Name the blood parasite species.
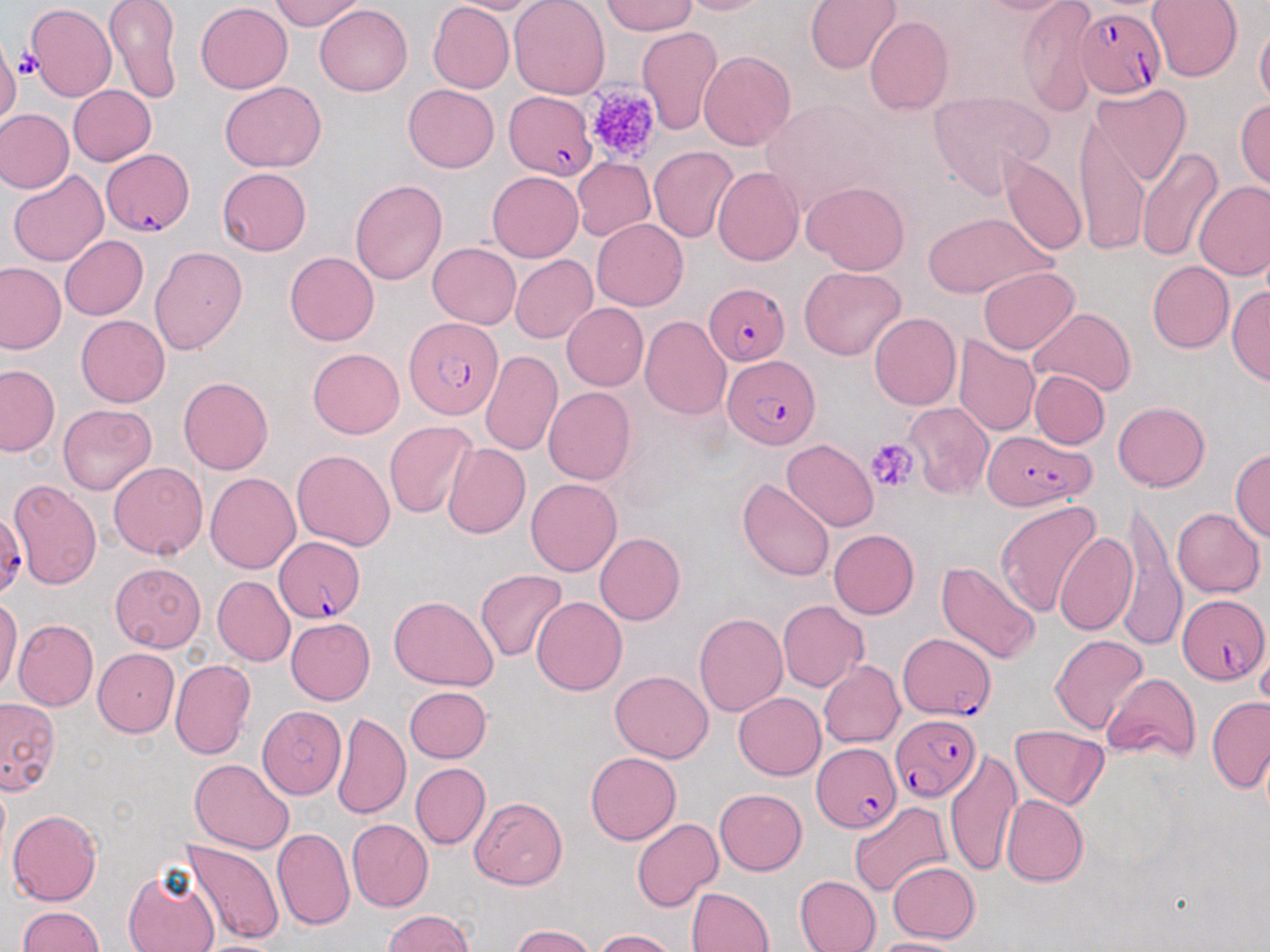

Plasmodium falciparum.

Approximate bounding boxes as [x1, y1, x2, y2] in pixels. Platelet locations: [15, 50, 39, 81], [582, 82, 664, 164], [866, 438, 919, 493]. Plasmodium falciparum-infected red blood cell locations: [1076, 7, 1165, 99], [503, 91, 597, 180], [102, 149, 194, 236], [703, 281, 789, 369], [404, 317, 505, 421], [722, 355, 819, 448], [983, 429, 1096, 510], [0, 512, 25, 597], [274, 536, 366, 622], [1178, 594, 1268, 685], [897, 633, 993, 719], [893, 711, 981, 802], [811, 741, 900, 833]. Uninfected red blood cell locations: [104, 0, 182, 104], [269, 0, 365, 31], [444, 0, 548, 14], [509, 0, 610, 100], [673, 0, 774, 15], [804, 0, 902, 74], [965, 0, 1079, 15], [1016, 0, 1098, 116], [1146, 0, 1242, 81], [196, 1, 293, 93], [428, 1, 514, 93], [602, 1, 698, 36], [26, 3, 116, 100], [315, 3, 412, 97], [865, 16, 953, 117], [1255, 20, 1270, 110], [636, 26, 724, 134], [0, 39, 20, 127], [698, 50, 797, 150], [219, 81, 327, 171], [404, 84, 499, 172], [1089, 84, 1191, 188], [69, 85, 156, 166], [928, 91, 1053, 196], [757, 98, 891, 214], [1234, 98, 1270, 190], [1, 109, 72, 193], [1074, 114, 1148, 255], [1136, 146, 1225, 262], [649, 147, 740, 244], [1000, 154, 1086, 258], [571, 156, 655, 242], [217, 167, 312, 255], [712, 167, 804, 266], [7, 171, 108, 266], [487, 171, 583, 262], [350, 179, 448, 285], [801, 181, 909, 274], [1193, 181, 1270, 281], [923, 211, 1053, 297], [591, 219, 687, 311], [60, 236, 148, 320], [427, 242, 521, 328], [149, 246, 247, 354], [284, 251, 379, 345], [510, 255, 597, 343], [1146, 260, 1235, 353], [0, 262, 65, 354], [799, 266, 906, 360], [977, 266, 1078, 354], [1226, 287, 1269, 386], [561, 302, 649, 390], [1029, 307, 1135, 396], [869, 312, 961, 411], [76, 315, 171, 407], [640, 315, 732, 419], [952, 335, 1040, 436], [307, 348, 405, 438], [479, 350, 562, 456], [0, 364, 59, 456], [1029, 370, 1109, 448], [178, 376, 273, 474], [543, 387, 637, 485], [904, 401, 993, 499], [1114, 401, 1210, 491], [58, 402, 156, 495], [384, 421, 478, 520], [782, 439, 878, 533], [443, 442, 530, 539], [1230, 448, 1270, 542], [292, 449, 395, 551], [108, 461, 208, 560], [205, 472, 300, 574], [736, 477, 836, 582], [526, 478, 622, 576], [8, 479, 102, 590], [1121, 497, 1185, 653], [994, 500, 1104, 620], [1172, 508, 1264, 597], [828, 529, 919, 619], [1055, 529, 1138, 637], [594, 532, 685, 625], [936, 561, 1041, 665], [110, 563, 206, 651], [475, 569, 566, 662], [213, 576, 295, 666], [0, 595, 22, 698], [388, 596, 499, 690], [531, 596, 627, 696], [778, 600, 869, 692], [694, 612, 788, 716], [285, 618, 375, 705], [13, 620, 98, 712], [1050, 634, 1149, 737], [1255, 639, 1270, 718], [94, 649, 179, 737], [170, 658, 256, 760], [818, 660, 905, 748], [610, 670, 714, 763], [1102, 674, 1201, 762], [404, 686, 492, 763], [733, 691, 826, 779], [1206, 697, 1270, 792], [0, 698, 60, 795], [257, 703, 347, 800], [332, 711, 411, 821], [1009, 725, 1109, 809], [945, 748, 1022, 877], [585, 750, 681, 845], [190, 758, 295, 853], [410, 763, 490, 848], [714, 788, 807, 875], [1002, 794, 1088, 887], [469, 797, 567, 889], [849, 801, 951, 897], [8, 809, 102, 906], [632, 818, 722, 912], [347, 819, 434, 911], [270, 826, 355, 929], [182, 839, 285, 946], [886, 861, 981, 942], [123, 869, 218, 952], [794, 875, 881, 952], [685, 887, 775, 951], [16, 906, 103, 952], [383, 909, 475, 952], [509, 925, 596, 952], [595, 929, 679, 952], [864, 937, 967, 952], [193, 939, 286, 952]. May-Grünwald-Giemsa stain. Thin blood smear. Image is 1270×952 pixels. One field of a larger specimen. 1000x magnification. Optical microscopy.